Describe the morphology of the red blood cells.
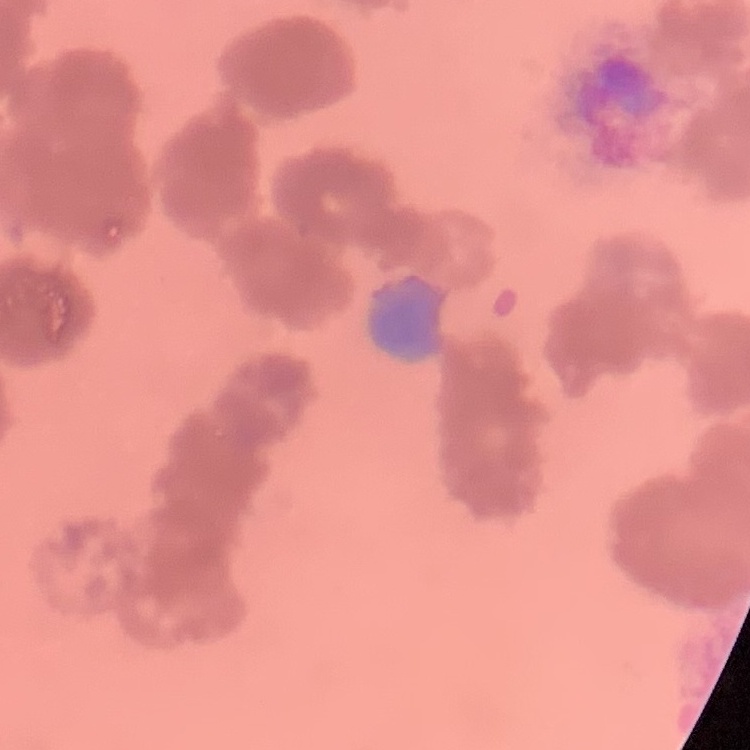

They show rouleaux formation.

Summary:
  - Stain: Field's or Giemsa
  - Preparation: thin blood film
  - Image type: one tile cut from a larger photomicrograph